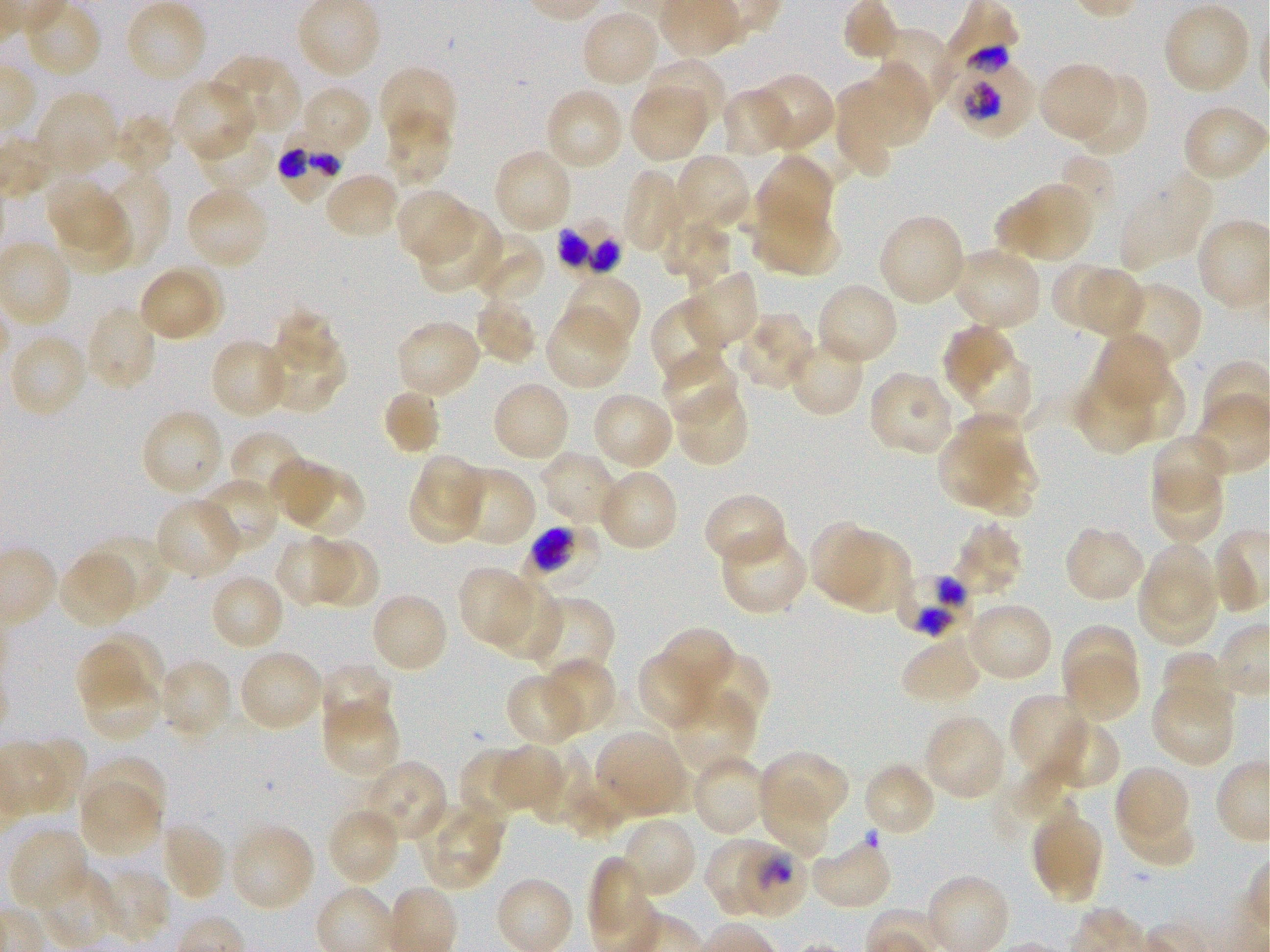

Approximate bounding boxes as [x1, y1, x2, y2] in pixels. Not every red blood cell is marked. A life-cycle stage — or a range of stages, where the recorded stages span more than one — follows each staged infected red blood cell.
Summary:
  - Locations of uninfected red blood cells: [124, 0, 208, 84], [842, 0, 898, 61], [1162, 3, 1252, 95], [581, 10, 660, 89], [873, 27, 952, 110], [213, 54, 303, 136], [642, 57, 727, 133], [1039, 63, 1118, 143], [857, 66, 930, 147], [378, 70, 454, 145], [750, 72, 835, 151], [1072, 73, 1147, 158], [171, 78, 256, 162], [832, 83, 898, 176], [299, 85, 371, 157], [630, 86, 707, 162], [543, 87, 625, 171], [722, 87, 791, 158], [34, 91, 120, 175], [1186, 110, 1270, 179], [383, 111, 452, 188], [113, 113, 176, 178], [194, 124, 277, 192], [492, 148, 573, 234], [673, 154, 753, 233], [755, 154, 833, 240], [1060, 156, 1116, 207], [621, 168, 688, 254], [94, 170, 171, 267], [324, 171, 399, 239], [1119, 175, 1213, 270], [47, 180, 123, 254], [1022, 183, 1094, 263], [185, 185, 269, 269], [395, 188, 471, 264], [55, 199, 133, 273], [995, 199, 1047, 255], [751, 203, 840, 278], [417, 210, 500, 293], [878, 215, 967, 306], [662, 220, 728, 286], [472, 231, 544, 305], [952, 247, 1043, 331], [1051, 263, 1112, 328], [161, 264, 225, 337], [686, 269, 761, 350], [1081, 269, 1141, 339], [141, 271, 214, 339], [562, 273, 642, 351], [813, 282, 899, 367], [1113, 283, 1203, 370], [649, 295, 728, 386], [472, 296, 540, 366], [85, 304, 158, 392], [273, 307, 337, 369], [545, 309, 631, 390], [734, 312, 815, 391], [395, 319, 482, 399], [943, 324, 1016, 399], [1094, 332, 1172, 410], [9, 333, 89, 418], [263, 333, 345, 413], [787, 336, 864, 417], [209, 337, 290, 420], [662, 353, 740, 427], [965, 353, 1033, 427], [1114, 367, 1185, 444], [871, 371, 953, 454], [1071, 372, 1155, 454], [490, 381, 571, 463], [382, 387, 442, 456], [678, 388, 746, 466], [591, 391, 674, 471], [140, 408, 226, 496], [939, 418, 1022, 507], [229, 430, 309, 504], [1151, 432, 1227, 509], [968, 445, 1038, 518], [540, 449, 621, 524], [420, 456, 483, 519], [271, 458, 339, 524], [597, 468, 679, 552], [1151, 470, 1223, 545], [459, 471, 537, 548], [290, 472, 366, 538], [198, 476, 280, 554], [410, 477, 486, 543], [703, 493, 784, 562], [155, 498, 242, 579], [954, 522, 1024, 597], [808, 523, 883, 604], [1068, 529, 1143, 599], [723, 532, 806, 613], [88, 534, 170, 614], [274, 535, 352, 608], [835, 536, 912, 614], [318, 539, 380, 605], [1143, 543, 1216, 624], [59, 552, 138, 629], [458, 566, 533, 646], [1139, 567, 1217, 646], [209, 574, 285, 652], [490, 579, 562, 661], [530, 595, 615, 683], [375, 596, 445, 668], [969, 607, 1050, 679], [1062, 624, 1139, 703], [660, 626, 735, 702], [101, 632, 164, 696], [901, 636, 979, 700], [76, 644, 141, 712], [238, 649, 324, 733], [637, 651, 714, 732], [696, 651, 769, 730], [1159, 651, 1229, 719], [1063, 654, 1137, 723], [542, 658, 618, 734], [159, 659, 233, 739], [318, 663, 391, 736], [80, 670, 163, 743], [505, 673, 585, 748], [1150, 684, 1235, 766], [669, 690, 757, 773], [1009, 694, 1094, 776], [321, 700, 400, 779], [923, 714, 1007, 800], [1051, 720, 1121, 787], [595, 730, 688, 817], [32, 737, 85, 811], [491, 745, 563, 811], [536, 745, 592, 825], [457, 747, 528, 822], [758, 750, 849, 828], [691, 752, 769, 836], [86, 755, 168, 827], [370, 762, 446, 838], [863, 762, 938, 839], [1115, 764, 1186, 837], [566, 781, 625, 841], [80, 784, 161, 857], [759, 785, 830, 857], [419, 800, 506, 890], [326, 806, 402, 886], [1118, 812, 1196, 866], [620, 817, 699, 901], [1034, 817, 1103, 903], [160, 822, 228, 902], [229, 823, 316, 913], [9, 829, 90, 913], [701, 835, 769, 917], [810, 837, 894, 912], [588, 855, 648, 935], [39, 868, 119, 947], [96, 868, 172, 944]
  - Locations of infected red blood cells: [947, 46, 1035, 138]; [278, 129, 345, 205]; [558, 221, 619, 273]; [527, 524, 604, 594] trophozoite; [899, 571, 971, 637]; [737, 846, 806, 917] trophozoite
  - Preparation: thin blood film
  - Culture: static in-vitro Plasmodium falciparum strain 3D7
  - Stain: Giemsa
  - Field of view: one from this slide
  - Donor blood group: O+
  - Objective: 100x, oil immersion, numerical aperture 1.25
  - Image size: 1270×952 pixels